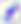

magnification: 400x
modality: photomicrograph
identification: Toxoplasma gondii